Identify the blood parasite species.
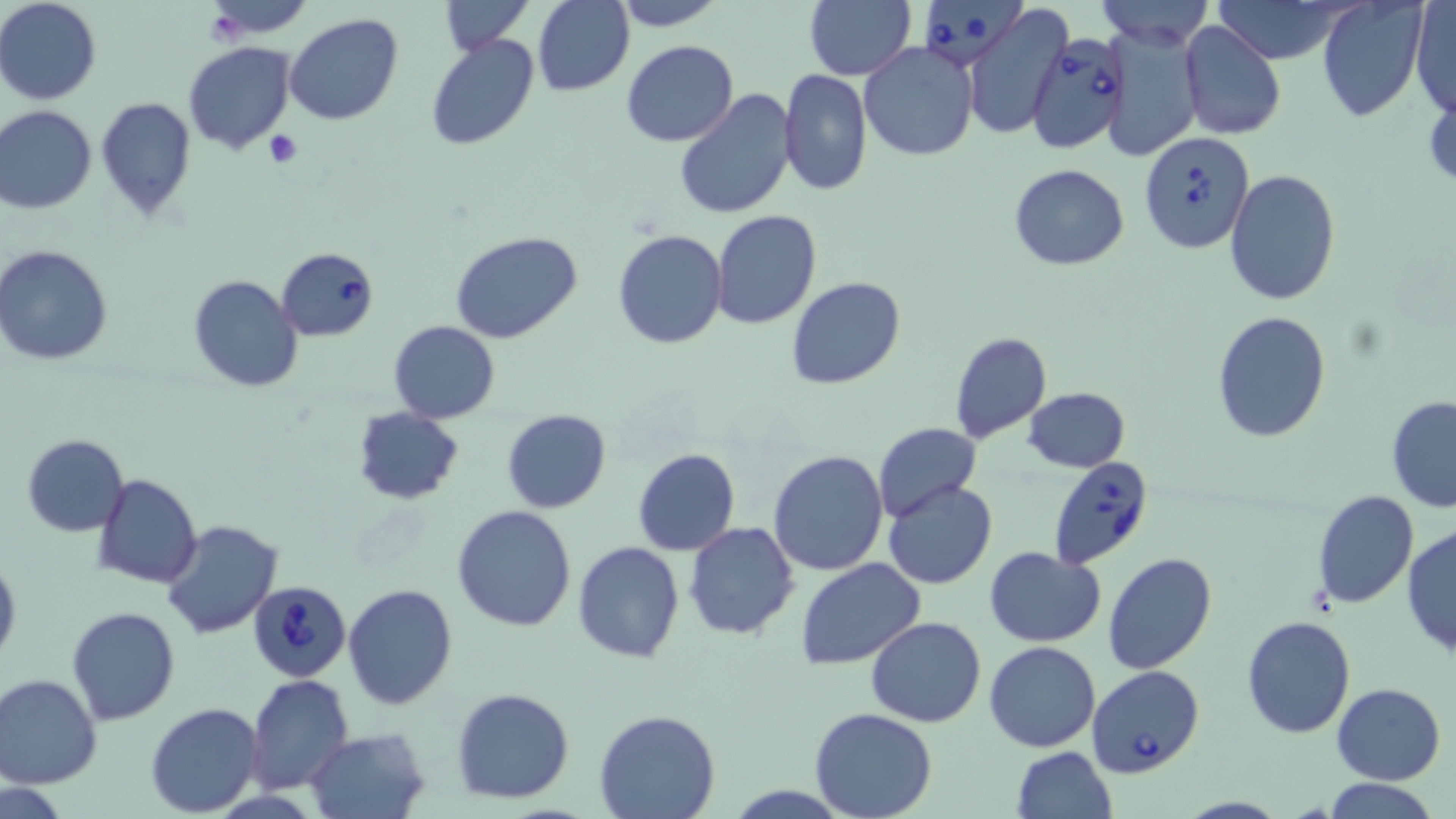

Babesia divergens.

stain: May-Grünwald-Giemsa
platelet_locations: 'approximate bounding boxes as (x1,y1)-(x2,y2) corner pairs in pixels: (265,131)-(302,169)'
modality: light microscopy
babesia_divergens_infected_red_blood_cell_locations: 'approximate bounding boxes as (x1,y1)-(x2,y2) corner pairs in pixels: (922,0)-(1030,70), (1026,32)-(1132,152), (1139,132)-(1254,254), (276,247)-(379,342), (1049,453)-(1154,569), (247,577)-(351,678), (1088,666)-(1205,777)'
image_size: 1456×819 pixels
preparation: thin blood smear
field_of_view: one of a larger specimen
magnification: 1000x
uninfected_red_blood_cell_locations: 'approximate bounding boxes as (x1,y1)-(x2,y2) corner pairs in pixels: (0,0)-(102,104), (202,0)-(313,37), (439,0)-(531,54), (611,0)-(726,30), (805,0)-(916,81), (1096,0)-(1213,49), (1208,0)-(1353,64), (1411,0)-(1455,120), (534,1)-(633,95), (1317,1)-(1428,122), (964,5)-(1071,140), (284,12)-(403,125), (1179,20)-(1285,140), (1100,22)-(1203,161), (424,34)-(539,152), (621,39)-(738,147), (183,42)-(296,154), (858,42)-(979,163), (778,69)-(872,195), (673,89)-(798,220), (95,97)-(198,221), (0,105)-(98,214), (1009,163)-(1129,270), (1225,168)-(1340,304), (712,209)-(820,329), (612,229)-(727,350), (451,230)-(584,346), (0,244)-(113,365), (189,274)-(304,392), (786,277)-(907,389), (1211,311)-(1331,443), (389,321)-(500,423), (948,331)-(1053,445), (1022,386)-(1130,473), (1386,396)-(1456,514), (353,407)-(465,505), (501,410)-(612,513), (872,421)-(981,524), (22,435)-(128,537), (632,448)-(740,556), (769,449)-(888,576), (94,474)-(202,589), (882,479)-(998,589), (1311,489)-(1419,609), (451,505)-(578,632), (161,518)-(285,640), (684,522)-(799,640), (1401,524)-(1456,660), (572,540)-(685,662), (984,547)-(1105,647), (0,549)-(21,671), (1103,553)-(1217,675), (796,558)-(925,671), (341,583)-(459,711), (65,606)-(181,726), (866,615)-(986,728), (1241,616)-(1356,738), (868,624)-(1102,736), (984,640)-(1102,752), (246,673)-(354,792), (0,675)-(102,789), (1332,683)-(1445,784), (450,687)-(576,804), (144,702)-(265,817), (809,708)-(938,819), (594,710)-(721,819), (305,727)-(432,819), (1011,746)-(1118,819), (1320,779)-(1442,818), (0,780)-(76,819)'